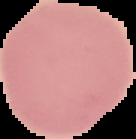
Summary:
  - Malaria status: uninfected
  - Image type: cell region segmented out of the field of view; surrounding area masked to black
  - Preparation: thin blood smear
  - Image size: 136×139 pixels